Report the malaria status of this cell.
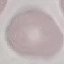

Uninfected.

stain: Giemsa
capture: smartphone through the microscope eyepiece
image_type: automatically extracted cell patch, resized to 64 × 64 pixels
preparation: thin blood film